Describe the morphology of the erythrocytes.
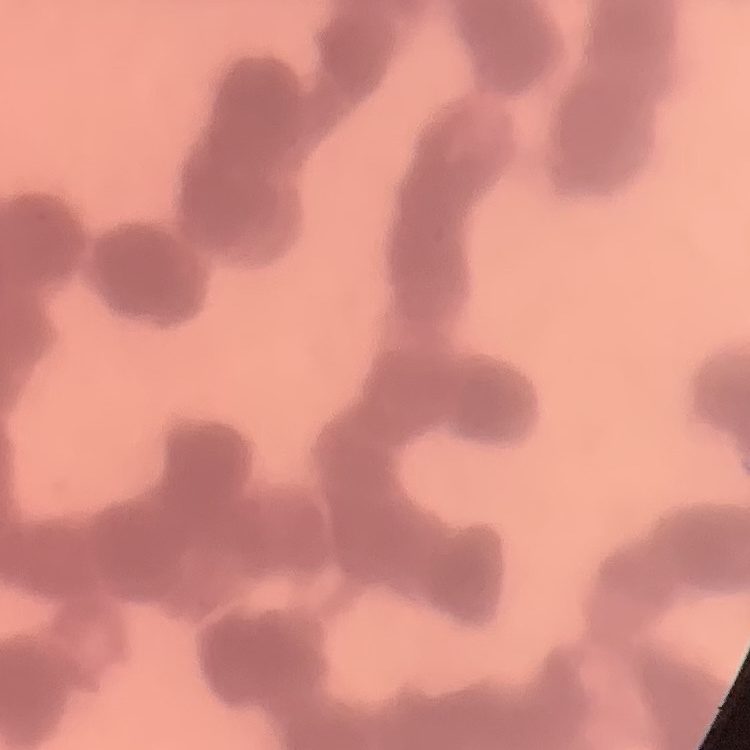
Rouleaux formation.

Summary:
  - Image type: square crop of a larger photomicrograph
  - Preparation: thin blood smear
  - Stain: Field's or Giemsa